Outline each blood parasite and name the species.
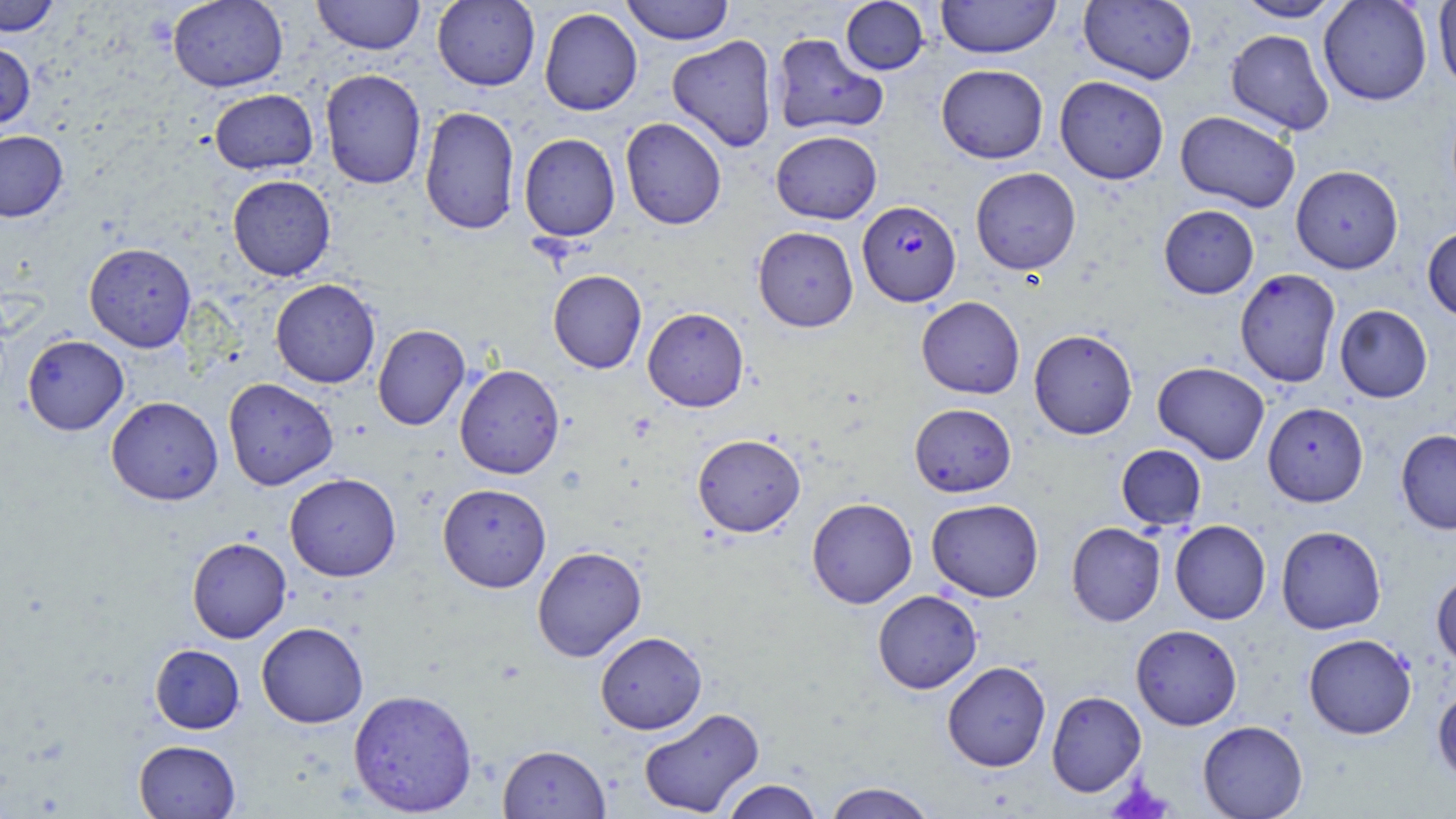
Approximate bounding boxes as [x1, y1, x2, y2] in pixels.
Plasmodium falciparum-infected red blood cells: [858, 200, 961, 306].
No Plasmodium ovale, Plasmodium malariae, Plasmodium vivax, Babesia divergens, or Trypanosoma brucei observed.

Uninfected red blood cell locations: [0, 0, 61, 36], [168, 0, 288, 92], [312, 0, 425, 55], [432, 0, 540, 91], [620, 0, 735, 45], [840, 0, 929, 75], [936, 0, 1060, 59], [1078, 0, 1198, 84], [1232, 0, 1348, 22], [1318, 0, 1432, 106], [1432, 0, 1456, 92], [539, 7, 642, 116], [1226, 29, 1334, 135], [770, 32, 888, 136], [667, 35, 778, 152], [0, 43, 36, 129], [936, 64, 1048, 163], [320, 69, 426, 189], [1054, 76, 1169, 184], [209, 77, 425, 179], [209, 89, 318, 174], [419, 106, 520, 235], [1175, 110, 1300, 212], [620, 117, 727, 229], [0, 130, 68, 222], [771, 130, 882, 224], [519, 133, 620, 241], [1290, 165, 1404, 273], [970, 167, 1081, 274], [227, 174, 336, 281], [1159, 204, 1259, 298], [753, 226, 859, 332], [1422, 226, 1456, 322], [84, 242, 196, 352], [1234, 268, 1341, 387], [548, 269, 647, 374], [270, 278, 381, 388], [916, 296, 1025, 398], [1334, 304, 1432, 402], [642, 307, 749, 412], [373, 324, 470, 431], [1028, 329, 1138, 439], [22, 334, 129, 435], [1152, 361, 1270, 464], [454, 364, 565, 479], [223, 378, 338, 490], [106, 396, 223, 505], [1262, 402, 1368, 506], [909, 403, 1016, 497], [1396, 430, 1456, 534], [692, 434, 806, 537], [1116, 444, 1206, 530], [285, 473, 401, 581], [437, 483, 551, 592], [806, 497, 917, 608], [926, 499, 1044, 602], [1170, 520, 1271, 624], [1066, 521, 1165, 626], [1276, 525, 1386, 634], [187, 536, 292, 643], [532, 546, 646, 662], [1431, 570, 1456, 669], [872, 590, 982, 694], [256, 622, 368, 728], [1130, 624, 1242, 730], [595, 631, 706, 734], [1303, 634, 1416, 739], [150, 644, 245, 733], [942, 661, 1051, 771], [1432, 685, 1456, 788], [348, 689, 478, 816], [1046, 690, 1146, 797], [638, 706, 764, 818], [1197, 720, 1308, 818], [133, 740, 241, 818], [497, 744, 611, 818], [720, 779, 823, 819], [822, 782, 939, 819]. Platelet locations: [1106, 779, 1175, 819]. Slide-level diagnosis: Plasmodium falciparum. Image is 1456×819 pixels. Light microscopy. One field of a larger specimen. May-Grünwald-Giemsa stain. Thin blood smear. Captured at 1000x magnification.